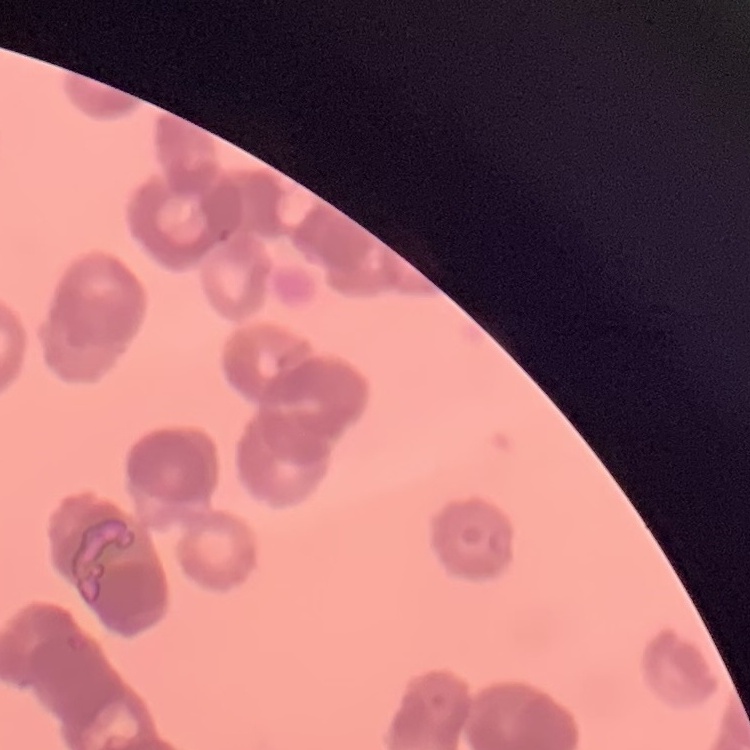
The erythrocytes show rouleaux formation. Thin peripheral smear. Field's or Giemsa stain. One tile cut from a larger photomicrograph.